Assess this cell for malaria.
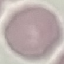
It is uninfected.

{
  "preparation": "thin blood smear",
  "stain": "Giemsa",
  "image_type": "automatically extracted cell patch, resized to 64 × 64 pixels",
  "capture": "smartphone camera at the microscope eyepiece"
}